Report the malaria status of this cell.
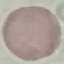
It is uninfected.

Summary:
  - Image type: automatically extracted cell patch, resized to 64 × 64 pixels
  - Stain: Giemsa
  - Capture: smartphone camera at the microscope eyepiece
  - Preparation: thin smear